Assess this cell for malaria.
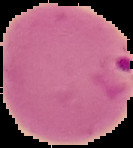

It is parasitized.

{
  "preparation": "thin blood smear",
  "image_size": "133×148 pixels",
  "image_type": "segmented cell region with the area outside set to black"
}